Identify the preparation type.
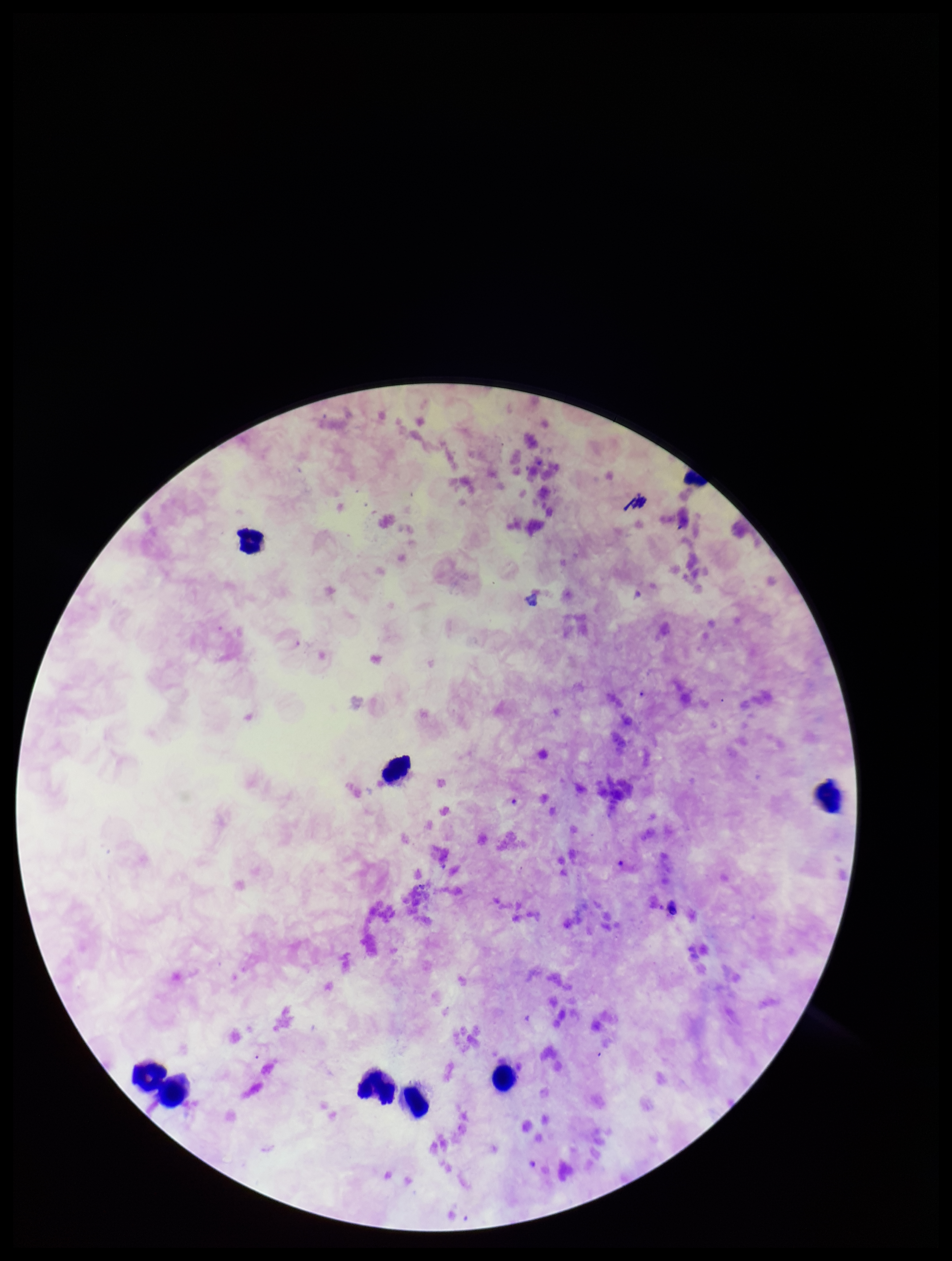

Thick.

Photographed through the microscope eyepiece with a smartphone camera. Patient malaria status: positive. Image is 952×1261 pixels. Single field of view. Parasite count: 0. Plasmodium parasites: none identified. Leukocyte count: 8. Species reported for this patient: Plasmodium falciparum. Stained with Giemsa.